State the blood parasite species.
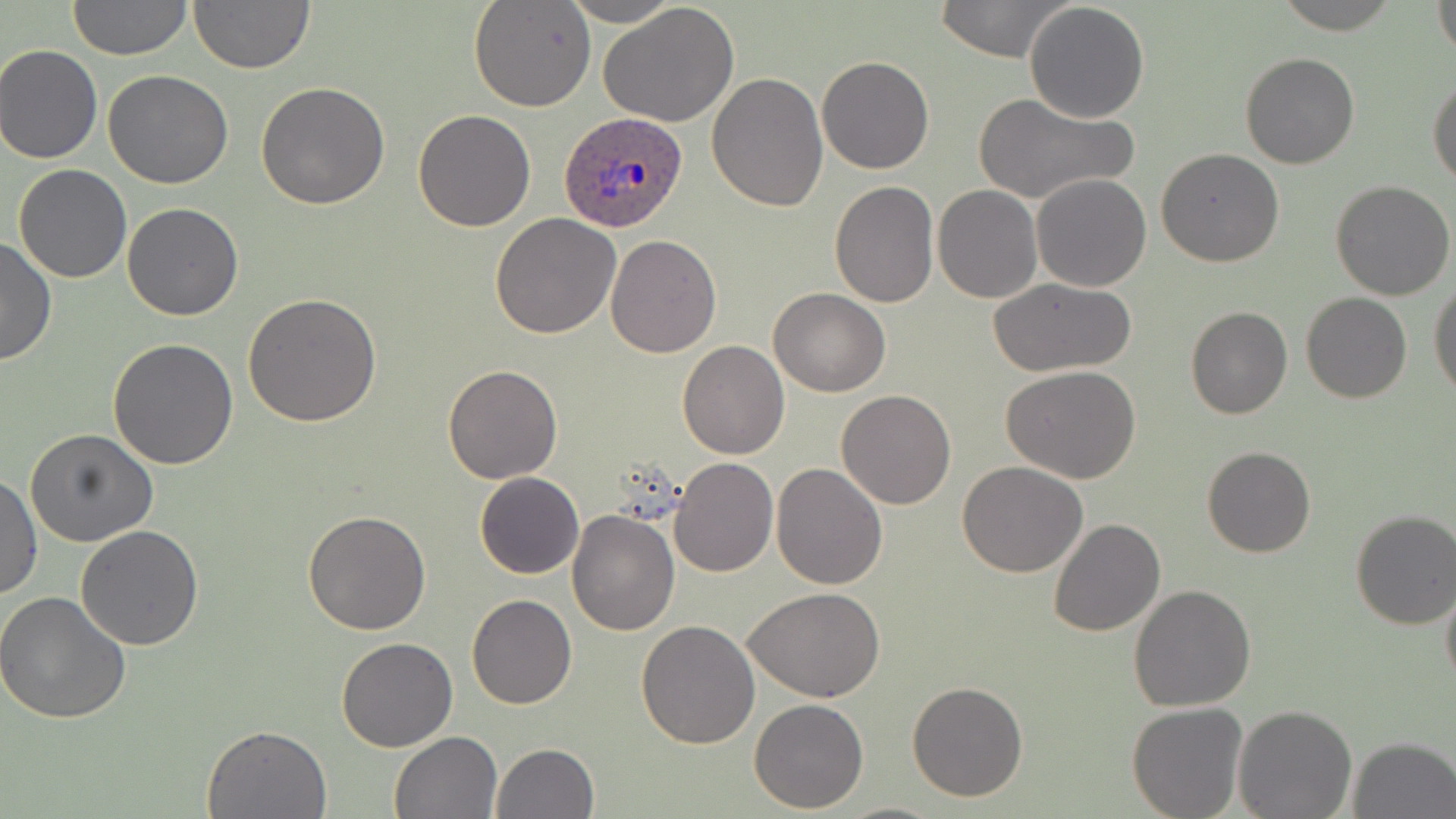
Plasmodium ovale.

field of view = one of a larger specimen
preparation = thin blood smear
uninfected red blood cell locations = approximate bounding boxes as (x1, y1, x2, y2) in pixels: (67, 0, 191, 60), (187, 0, 314, 73), (560, 0, 682, 27), (934, 0, 1073, 63), (1024, 0, 1150, 121), (468, 1, 596, 112), (1432, 1, 1455, 60), (598, 2, 740, 128), (0, 44, 104, 164), (1239, 51, 1360, 169), (817, 56, 934, 174), (103, 69, 234, 188), (1427, 72, 1456, 187), (707, 73, 829, 212), (256, 83, 390, 210), (971, 91, 1138, 205), (412, 109, 536, 231), (1156, 147, 1284, 267), (11, 165, 133, 284), (1031, 173, 1152, 292), (1330, 180, 1456, 300), (829, 181, 938, 306), (934, 185, 1042, 302), (121, 202, 243, 322), (490, 213, 620, 339), (605, 234, 722, 357), (0, 235, 56, 367), (986, 276, 1136, 378), (1429, 279, 1456, 400), (770, 288, 891, 397), (1301, 291, 1412, 404), (245, 293, 382, 427), (1186, 307, 1293, 420), (108, 337, 238, 470), (677, 340, 790, 459), (443, 363, 563, 483), (1001, 364, 1142, 483), (837, 390, 955, 511), (27, 428, 158, 547), (1202, 445, 1315, 558), (670, 457, 778, 577), (957, 461, 1087, 578), (770, 463, 887, 590), (1, 470, 41, 601), (475, 472, 584, 580), (1349, 509, 1456, 629), (302, 510, 431, 634), (567, 510, 680, 636), (1047, 519, 1165, 637), (76, 524, 203, 649), (1440, 580, 1456, 691), (743, 585, 886, 702), (1128, 585, 1257, 712), (0, 591, 132, 723), (467, 594, 577, 709), (637, 621, 760, 750), (334, 639, 457, 753), (906, 680, 1029, 803), (749, 698, 868, 813), (1126, 702, 1249, 819), (1233, 706, 1358, 819), (203, 723, 332, 818), (389, 731, 504, 819), (1347, 736, 1456, 819), (490, 743, 599, 819)
image size = 1456×819 pixels
Plasmodium ovale-infected red blood cell locations = approximate bounding boxes as (x1, y1, x2, y2) in pixels: (559, 110, 690, 232)
modality = optical microscopy
stain = May-Grünwald-Giemsa
magnification = 1000x